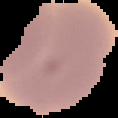 Image is 118×118 pixels. Malaria status: uninfected. From a thin blood film. The area outside the segmented cell region is set to black.